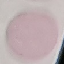
malaria status = uninfected
preparation = thin smear
stain = Giemsa
capture = smartphone camera at the microscope eyepiece
image type = cell patch, automatically extracted from a larger field of view and resized to 64 × 64 pixels